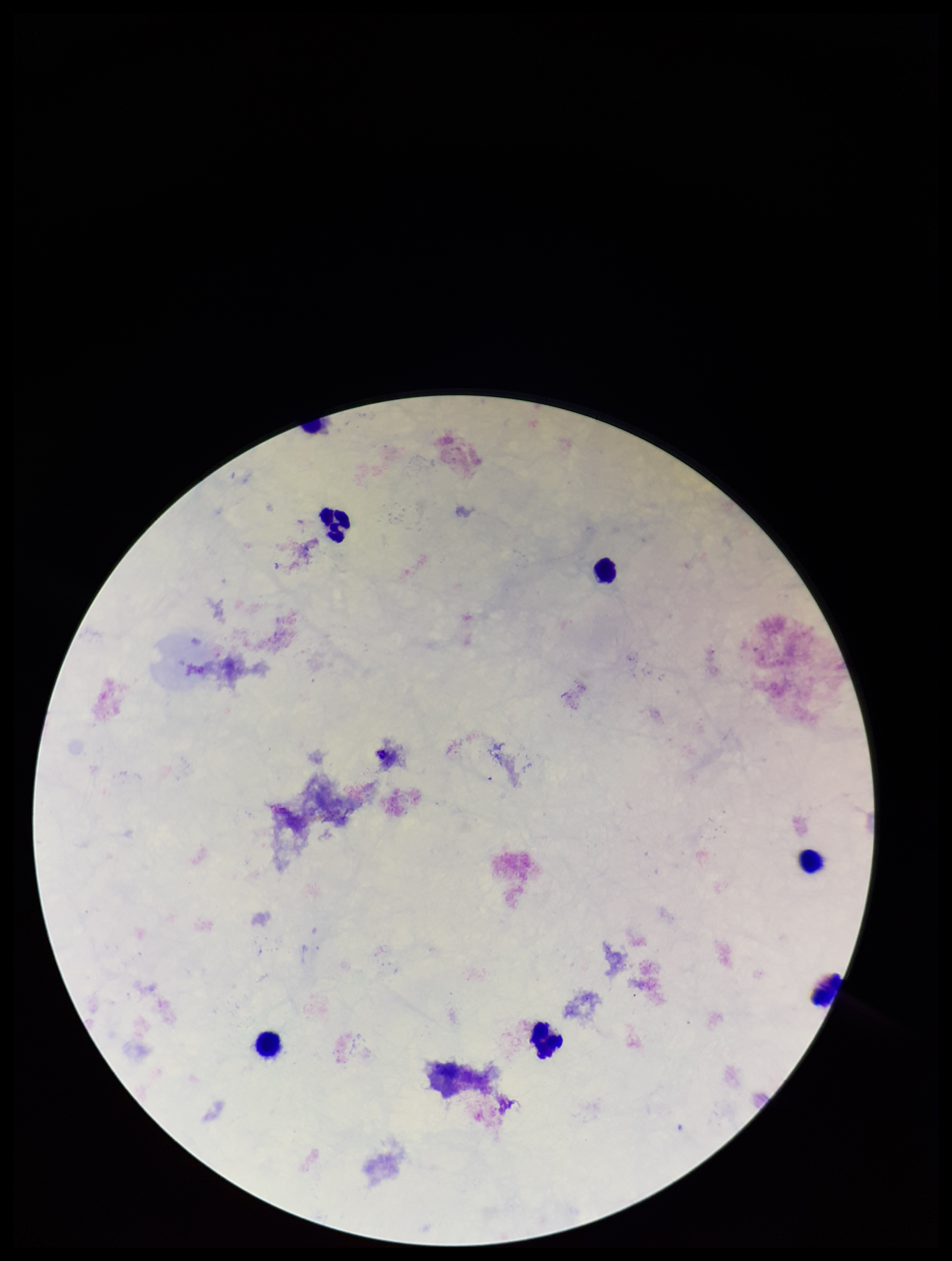
Plasmodium parasites: none detected. Single field of view. Image is 952×1261 pixels. Stained with Giemsa. Leukocyte count: 6. Photographed through the microscope eyepiece with a smartphone camera. Patient malaria status: negative. Parasite count: 0. Preparation: thick blood smear.